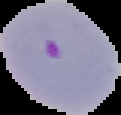 From a thin blood smear. Image is 121×115 pixels. Segmented cell region on a black background. Malaria status: parasitized.